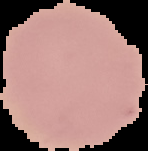

malaria status = uninfected
preparation = thin blood smear
image type = cell region segmented out of the field of view; surrounding area masked to black
image size = 148×151 pixels